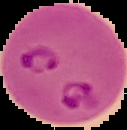
Image is 127×130 pixels. Result: Plasmodium parasites identified. From a thin blood smear. The area outside the segmented cell region is set to black.